Classify this cell by malaria status.
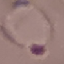
Parasitized.

Summary:
  - Preparation: thin blood smear
  - Image type: automatically extracted cell patch, resized to 64 × 64 pixels
  - Capture: smartphone through the microscope eyepiece
  - Stain: Giemsa